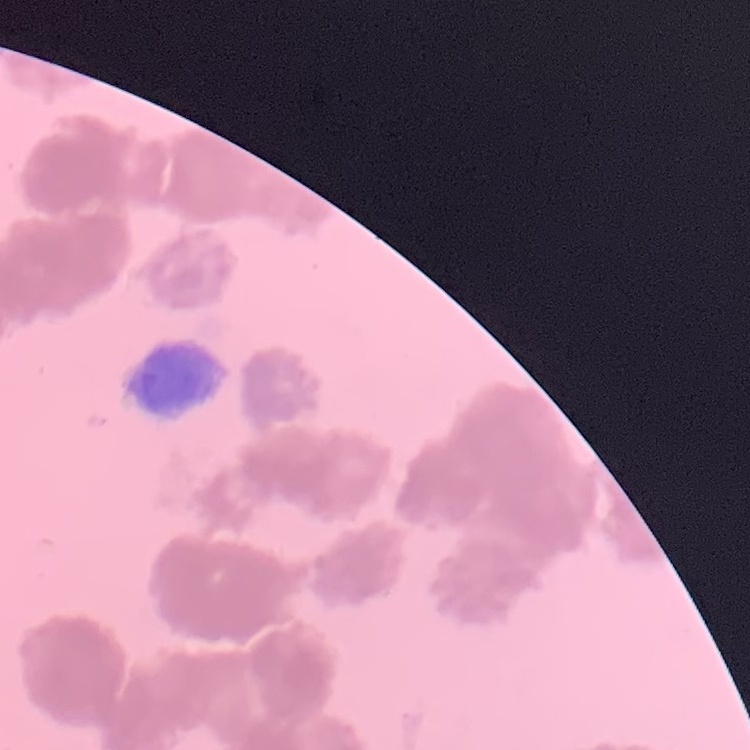
Summary:
  - Erythrocyte morphology: rouleaux formation
  - Stain: Field's or Giemsa
  - Image type: square crop of a larger photomicrograph
  - Preparation: thin blood smear